Assess this cell for malaria.
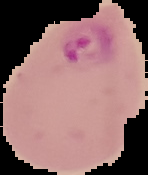

Parasitized.

preparation = thin blood film
image type = segmented cell region on a black background
image size = 148×175 pixels